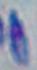

{
  "magnification": "1000x",
  "identification": "Toxoplasma gondii",
  "modality": "micrograph"
}